Assess the morphology of the red blood cells.
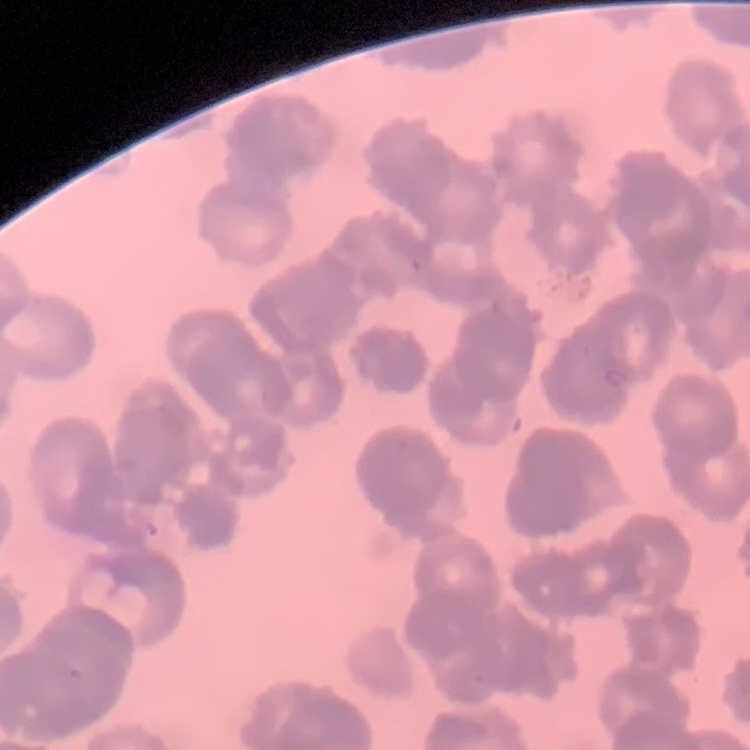

Rouleaux formation.

preparation = thin blood film
image type = square crop of a larger photomicrograph
stain = Field's or Giemsa